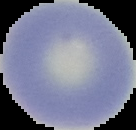
image_type: segmented cell region on a black background
image_size: 136×130 pixels
preparation: thin blood film
malaria_status: uninfected